Assess the morphology of the red blood cells.
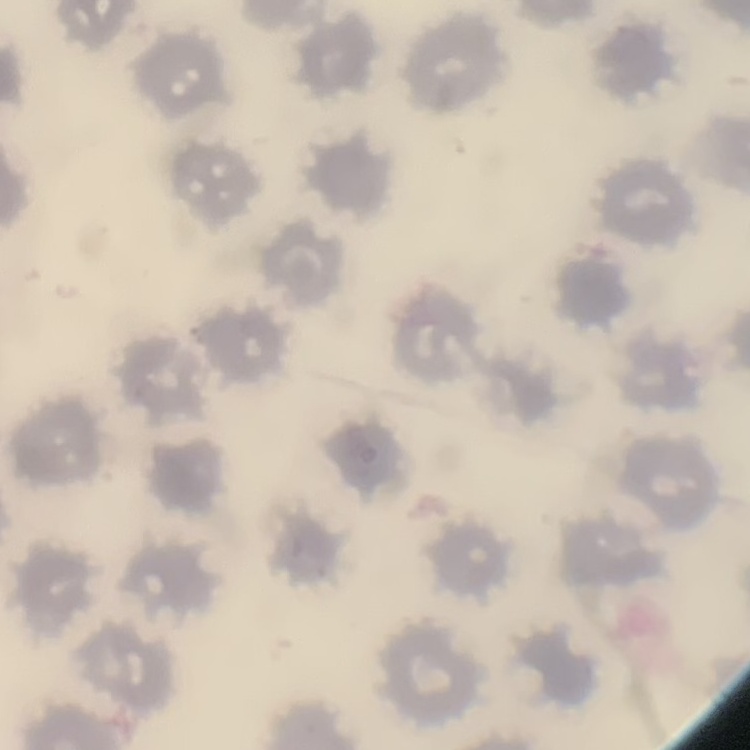
No rouleaux formation.

{
  "stain": "Field's or Giemsa",
  "preparation": "thin blood smear",
  "image_type": "one tile cut from a larger photomicrograph"
}